Report the malaria status of this cell.
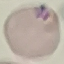

It is parasitized.

preparation: thin smear
capture: smartphone through the microscope eyepiece
stain: Giemsa
image_type: cell patch, automatically extracted from a larger field of view and resized to 64 × 64 pixels